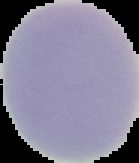
Segmented cell region on a black background. Image is 139×163 pixels. Malaria status: uninfected. From a thin blood film.